Classify this cell by malaria status.
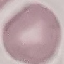
Uninfected.

Summary:
  - Image type: automatically extracted cell patch, resized to 64 × 64 pixels
  - Preparation: thin blood smear
  - Stain: Giemsa
  - Capture: smartphone camera at the microscope eyepiece